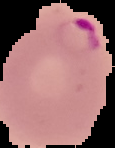

Summary:
  - Result: Plasmodium parasites detected
  - Preparation: thin blood smear
  - Image type: segmented cell region on a black background
  - Image size: 115×148 pixels